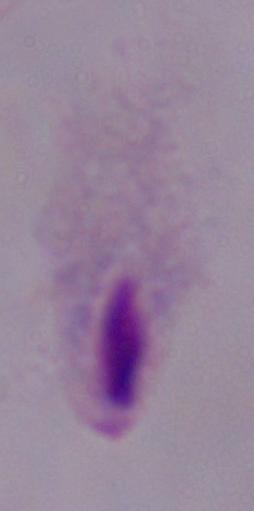

Summary:
  - Modality: micrograph
  - Magnification: 1000x
  - Identification: trichomonad